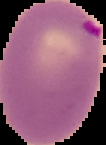
{
  "malaria_status": "parasitized",
  "image_size": "106×145 pixels",
  "image_type": "segmented cell region with the area outside set to black",
  "preparation": "thin blood film"
}